Report the malaria status.
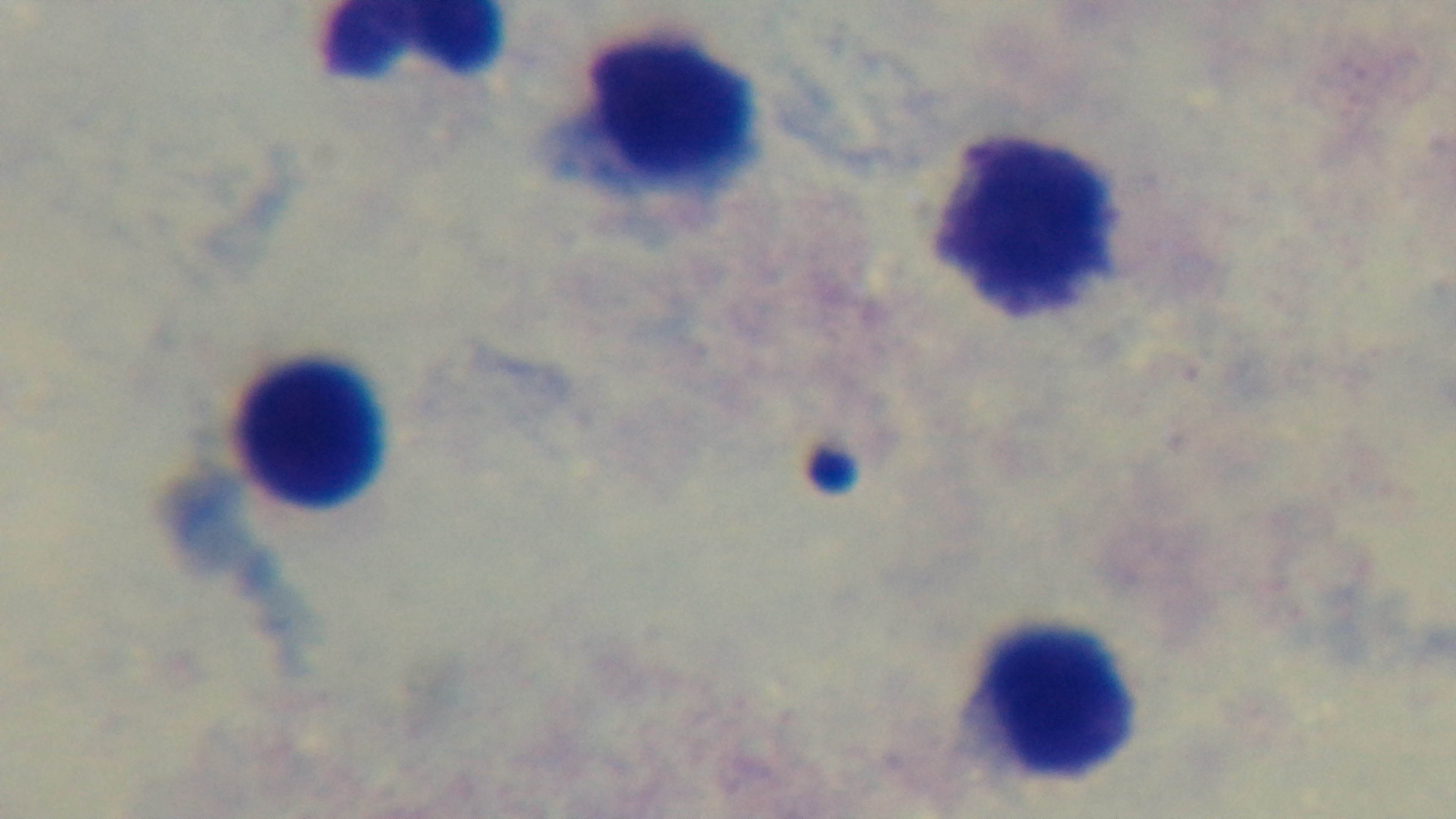

It is uninfected.

objective = 100x oil immersion
modality = light microscopy
preparation = thick
capture = mounted 4K digital camera
field of view = one from the slide
stain = Giemsa